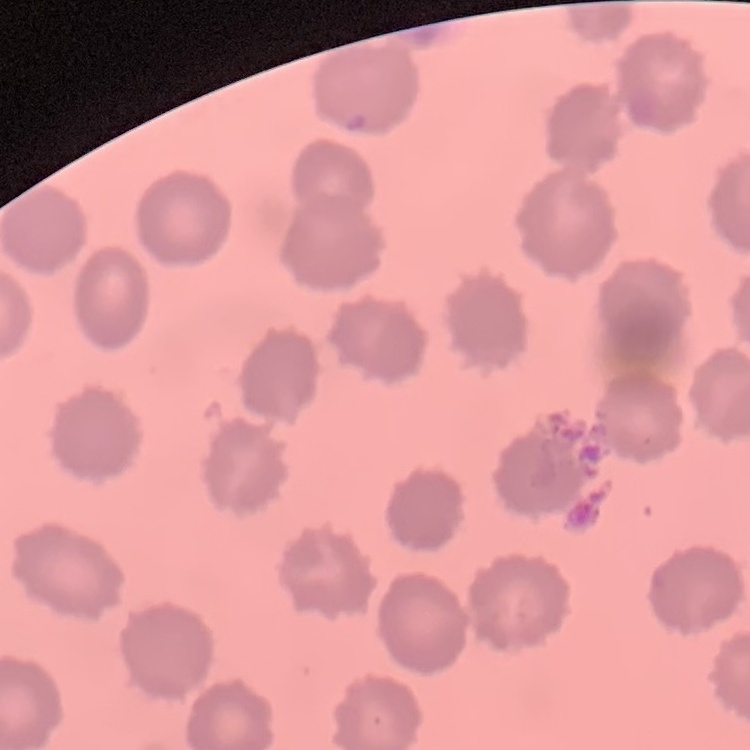

{
  "erythrocyte_morphology": "no rouleaux formation",
  "stain": "Field's or Giemsa",
  "image_type": "square crop of a larger photomicrograph",
  "preparation": "thin peripheral smear"
}